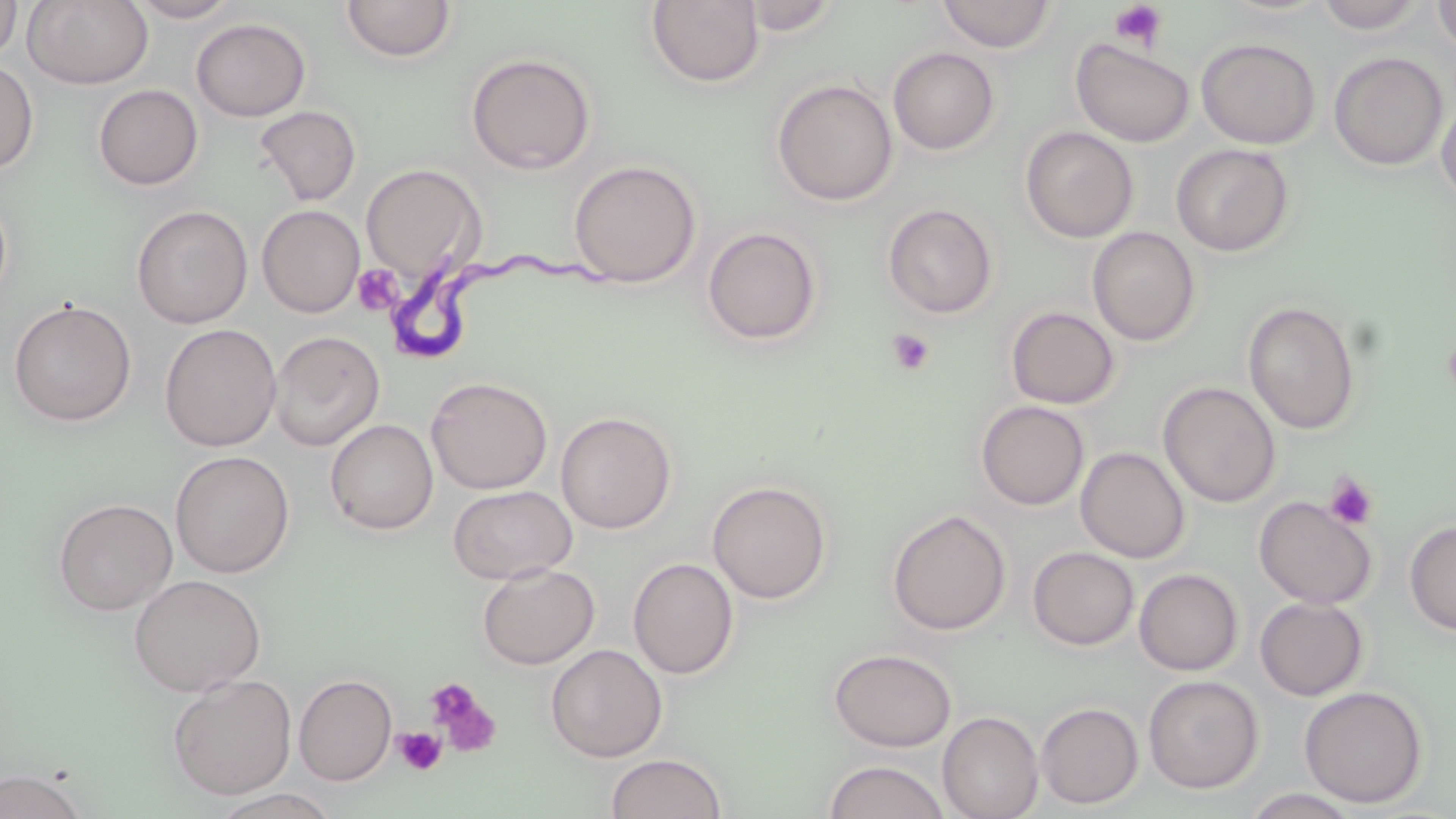
Summary:
  - Coordinate format: approximate bounding boxes as [x1, y1, x2, y2] in pixels
  - Trypanosoma brucei locations: [383, 239, 622, 356]
  - Platelet locations: [1107, 2, 1170, 52], [352, 265, 402, 316], [885, 329, 935, 377], [1442, 330, 1456, 403], [1324, 472, 1379, 530], [426, 679, 501, 757], [393, 727, 446, 775]
  - Uninfected red blood cell locations: [0, 0, 22, 62], [23, 0, 154, 90], [125, 0, 241, 22], [1315, 0, 1428, 33], [1432, 0, 1456, 55], [341, 1, 457, 63], [645, 1, 765, 88], [737, 1, 844, 36], [935, 1, 1057, 52], [191, 18, 310, 121], [1196, 37, 1321, 149], [1070, 38, 1196, 148], [888, 47, 1000, 155], [1328, 51, 1449, 171], [465, 53, 596, 174], [0, 60, 39, 174], [772, 78, 898, 206], [93, 83, 203, 190], [1436, 95, 1456, 207], [254, 105, 361, 206], [1020, 126, 1139, 243], [1171, 143, 1295, 256], [568, 159, 702, 288], [360, 163, 484, 282], [0, 192, 13, 309], [882, 203, 999, 319], [131, 204, 253, 328], [257, 204, 365, 317], [702, 225, 822, 346], [1087, 226, 1200, 346], [8, 298, 137, 427], [1243, 301, 1362, 435], [1005, 306, 1120, 409], [159, 323, 282, 452], [269, 330, 385, 451], [425, 376, 552, 495], [1158, 381, 1280, 507], [975, 400, 1089, 510], [555, 411, 677, 534], [324, 418, 439, 535], [1076, 446, 1190, 563], [170, 450, 294, 578], [707, 480, 832, 604], [447, 485, 577, 584], [1253, 495, 1378, 609], [52, 497, 178, 616], [886, 508, 1011, 636], [1404, 519, 1456, 636], [1028, 547, 1139, 650], [628, 557, 739, 679], [477, 563, 600, 669], [1134, 568, 1243, 675], [128, 574, 266, 697], [1255, 597, 1369, 701], [545, 644, 667, 763], [828, 648, 957, 752], [167, 674, 297, 801], [294, 674, 397, 785], [1143, 675, 1264, 794], [1298, 686, 1429, 808], [1035, 702, 1144, 809], [937, 711, 1044, 819], [605, 753, 727, 818], [822, 760, 951, 819], [0, 768, 89, 819], [209, 788, 339, 819], [1242, 788, 1362, 818]
  - Slide-level diagnosis: Trypanosoma brucei
  - Modality: optical microscopy
  - Stain: May-Grünwald-Giemsa
  - Image size: 1456×819 pixels
  - Field of view: single
  - Preparation: thin blood smear
  - Magnification: 1000x